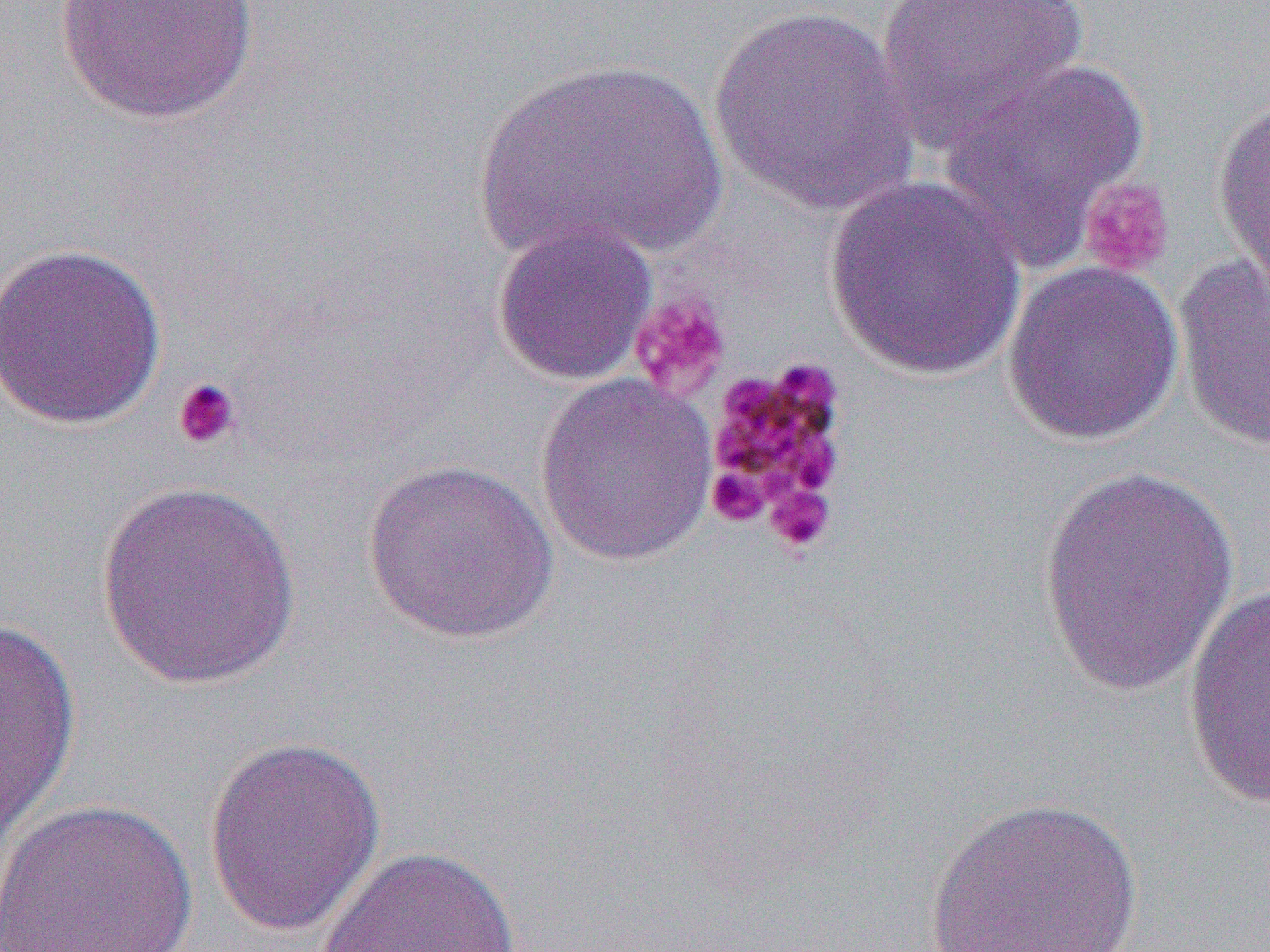
slide-level diagnosis = Plasmodium malariae
uninfected red blood cell locations = approximate bounding boxes as (x1,y1)-(x2,y2) corner pairs in pixels: (53,0)-(260,125), (874,0)-(1090,151), (708,5)-(920,215), (470,56)-(731,266), (936,57)-(1150,268), (1212,93)-(1270,302), (823,176)-(1029,380), (490,220)-(658,386), (0,241)-(168,431), (1173,253)-(1270,453), (1002,259)-(1184,446), (535,373)-(719,566), (361,456)-(560,644), (1036,466)-(1236,697), (94,480)-(303,691), (1183,584)-(1270,814), (0,617)-(81,854), (202,735)-(386,937), (922,795)-(1146,952), (2,798)-(199,951), (315,845)-(523,952)
field of view = single
modality = optical microscopy
preparation = thin blood film
platelet locations = approximate bounding boxes as (x1,y1)-(x2,y2) corner pairs in pixels: (1078,177)-(1175,278), (629,291)-(732,401), (702,357)-(854,527), (171,377)-(242,451), (706,465)-(770,527), (763,482)-(835,555)
image size = 1270×952 pixels
magnification = 1000x